Locate and identify every blood parasite.
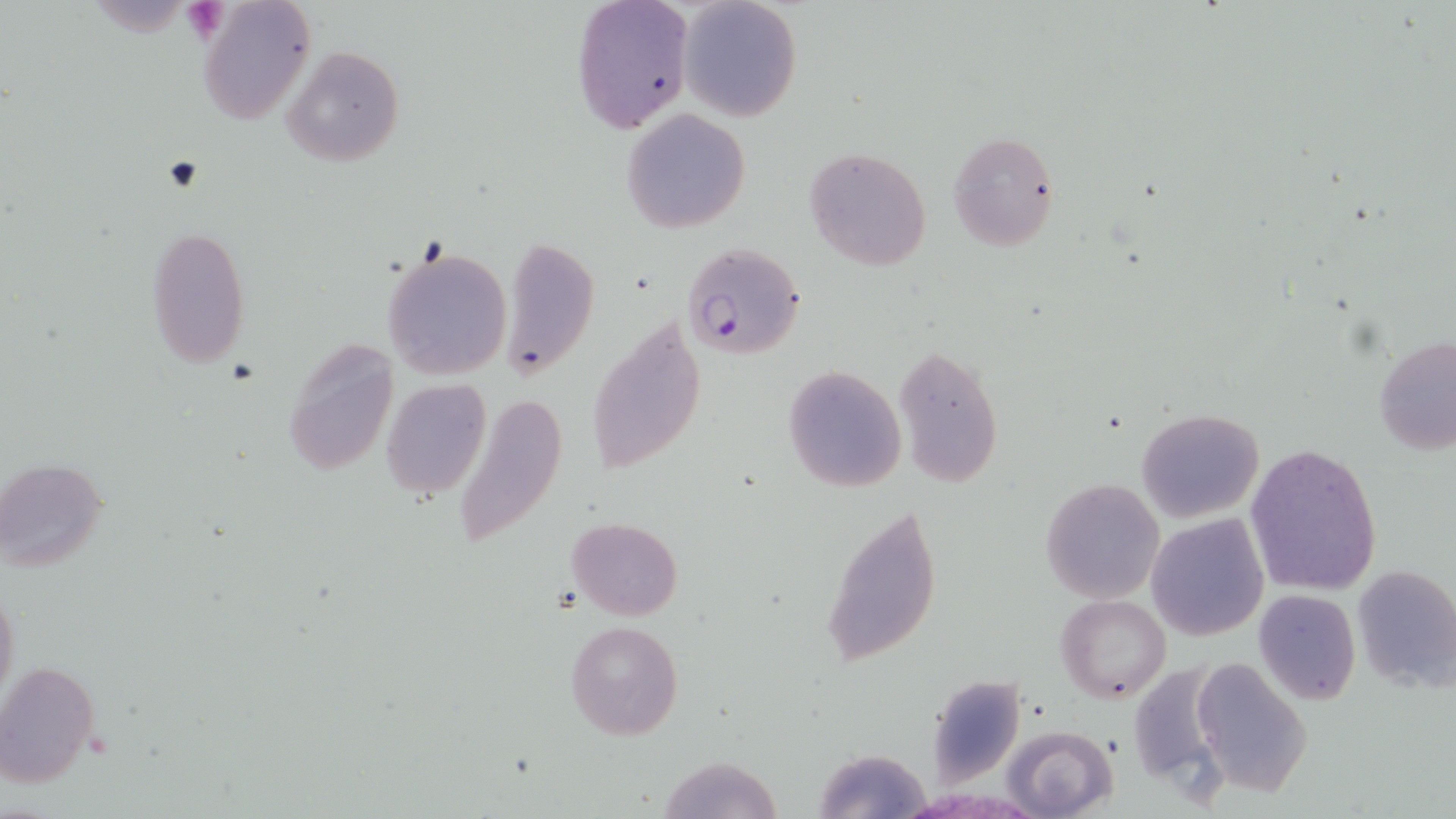
Approximate bounding boxes as [x1, y1, x2, y2] in pixels.
Plasmodium falciparum-infected red blood cells: [683, 240, 806, 360].
No Plasmodium ovale, Plasmodium malariae, Plasmodium vivax, Babesia divergens, or Trypanosoma brucei observed.

Summary:
  - Platelet locations: [183, 1, 229, 42]
  - Uninfected red blood cell locations: [570, 0, 692, 134], [677, 0, 802, 121], [197, 2, 315, 124], [283, 45, 403, 167], [621, 108, 751, 233], [946, 131, 1061, 250], [804, 146, 932, 272], [146, 225, 251, 365], [502, 235, 598, 383], [381, 244, 512, 381], [587, 313, 708, 477], [1374, 334, 1456, 457], [282, 335, 400, 477], [893, 343, 1004, 488], [782, 365, 906, 494], [380, 379, 491, 499], [451, 391, 570, 549], [1135, 409, 1265, 522], [1246, 445, 1382, 596], [1, 459, 108, 573], [1040, 477, 1165, 603], [821, 501, 943, 671], [1146, 512, 1269, 642], [566, 516, 683, 620], [1351, 562, 1456, 693], [0, 584, 19, 708], [1253, 589, 1362, 706], [1056, 595, 1171, 702], [565, 619, 683, 739], [1190, 658, 1314, 795], [1130, 660, 1229, 789], [0, 661, 101, 787], [925, 674, 1024, 784], [1005, 725, 1118, 818], [814, 747, 932, 819], [656, 755, 780, 818]
  - Slide-level diagnosis: Plasmodium falciparum
  - Stain: May-Grünwald-Giemsa
  - Modality: optical microscopy
  - Magnification: 1000x
  - Image size: 1456×819 pixels
  - Field of view: one of a larger specimen
  - Preparation: thin blood film